State which parasite is depicted.
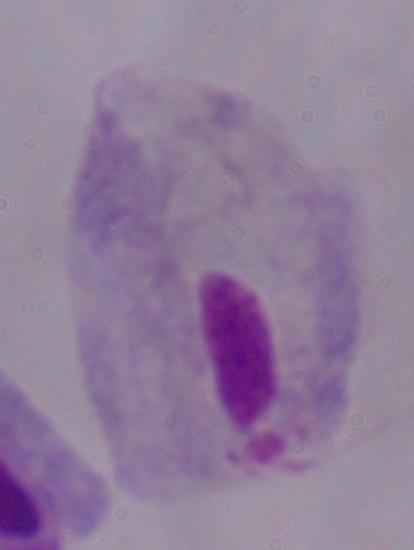

This is a trichomonad.

Micrograph. 1000x magnification.